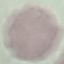 Result: no malaria parasites detected. Giemsa-stained preparation. Automatically extracted cell patch, resized to 64 × 64 pixels. Photographed with a smartphone camera at the microscope eyepiece. Thin blood smear.